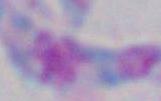
identification = Toxoplasma gondii
magnification = 1000x
modality = micrograph